Assess this cell for malaria.
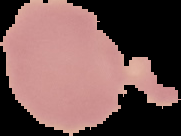

It is uninfected.

From a thin blood film. Segmented cell region on a black background. Image is 181×136 pixels.